Locate every Plasmodium parasite.
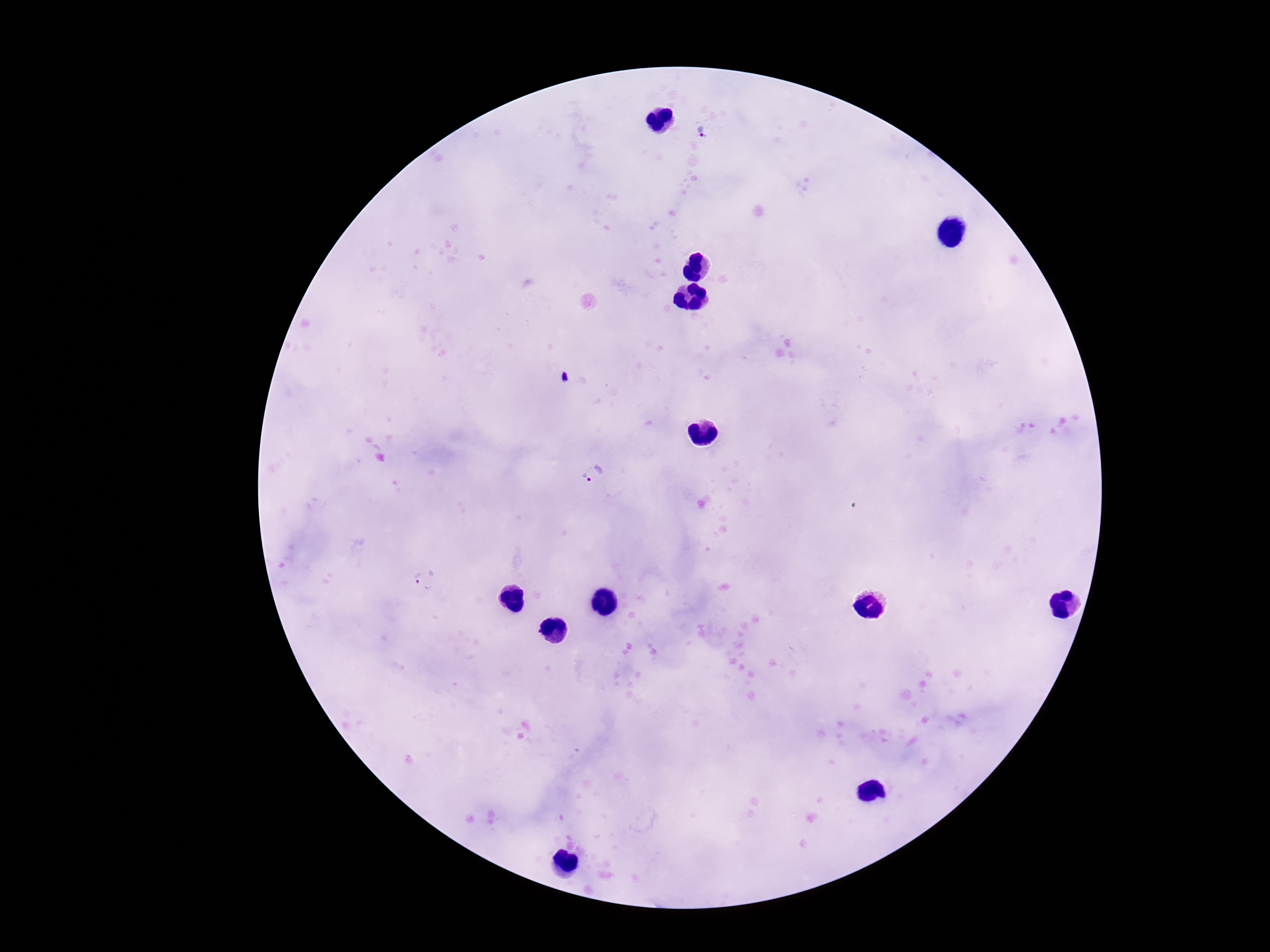
Approximate centers as (x, y) in pixels.
Plasmodium parasites: (707, 133), (564, 377), (585, 477).

Summary:
  - Patient malaria status: positive
  - Field of view: single
  - Magnification: 100x
  - Capture: smartphone camera through the microscope eyepiece
  - Stain: Giemsa
  - Image size: 1270×952 pixels
  - Preparation: thick blood smear